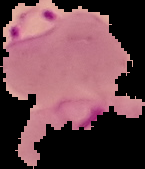
Summary:
  - Malaria status: parasitized
  - Image size: 145×169 pixels
  - Preparation: thin blood smear
  - Image type: segmented cell region with the area outside set to black